State which parasite is depicted.
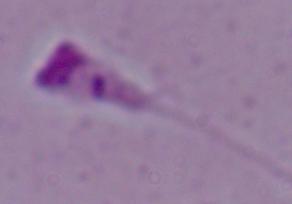

This is Leishmania.

Summary:
  - Modality: photomicrograph
  - Magnification: 1000x